Name the parasite shown.
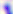
This is Toxoplasma gondii.

modality: photomicrograph
magnification: 400x